Classify this cell by malaria status.
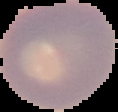

Uninfected.

image size = 118×112 pixels
image type = segmented cell region on a black background
preparation = thin blood film